Locate and identify every blood parasite.
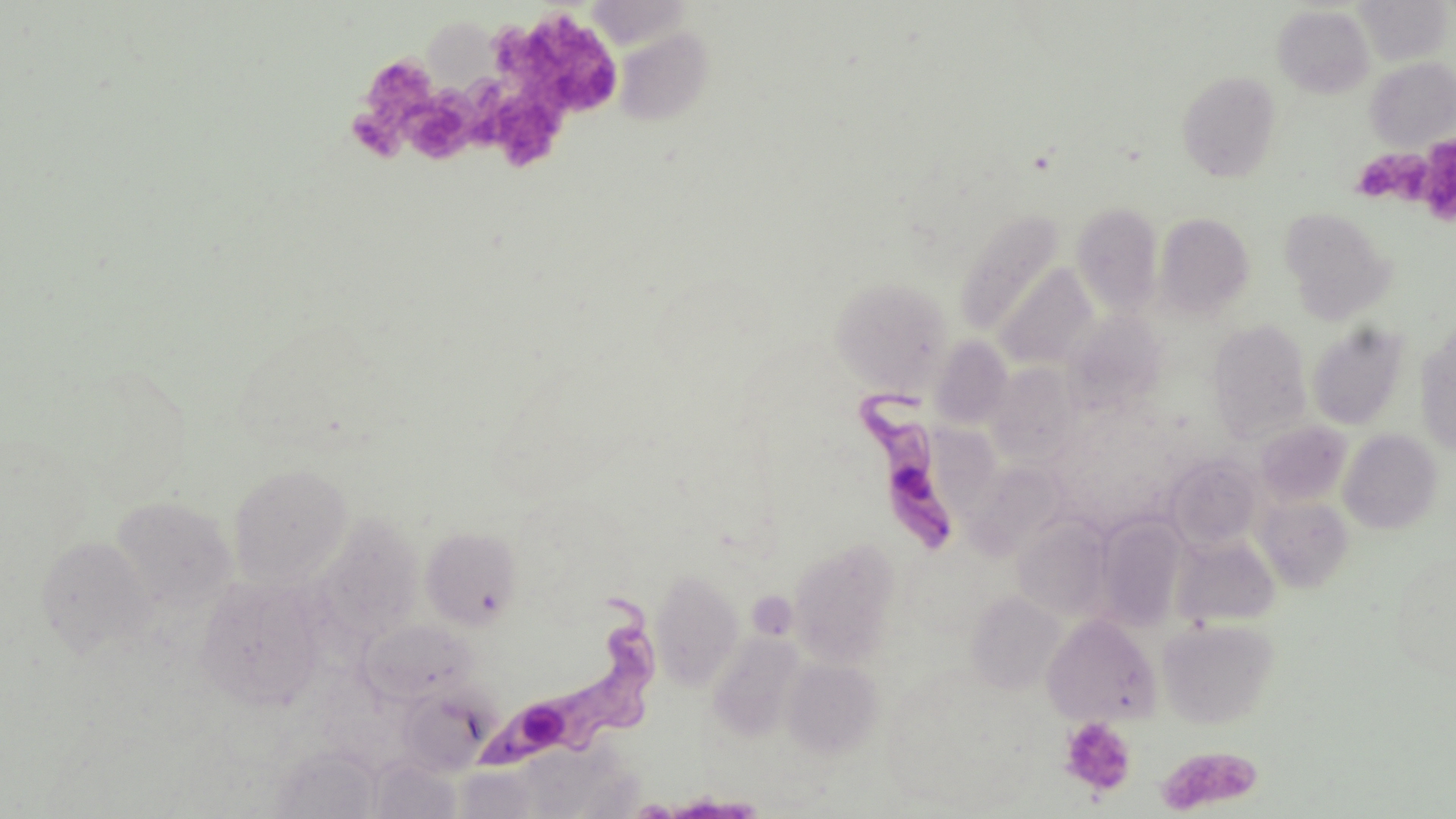

Approximate bounding boxes as (x1, y1, x2, y2) in pixels.
Trypanosoma brucei: (850, 385, 959, 558), (491, 595, 657, 769).
No Plasmodium falciparum, Plasmodium ovale, Plasmodium malariae, Plasmodium vivax, or Babesia divergens observed.

slide_level_diagnosis: Trypanosoma brucei
preparation: thin blood film
platelet_locations: 'approximate bounding boxes as (x1, y1, x2, y2) in pixels: (492, 9, 618, 116), (363, 55, 437, 117), (475, 85, 568, 171), (402, 94, 475, 164), (353, 108, 409, 164), (1417, 134, 1456, 223), (1353, 148, 1437, 208), (1059, 716, 1137, 797), (1157, 745, 1263, 815)'
uninfected_red_blood_cell_locations: 'approximate bounding boxes as (x1, y1, x2, y2) in pixels: (1356, 0, 1451, 65), (1273, 5, 1374, 97), (426, 13, 505, 94), (614, 27, 714, 126), (1366, 57, 1456, 150), (1177, 71, 1282, 181), (1071, 202, 1164, 315), (1279, 208, 1396, 323), (955, 209, 1065, 336), (1153, 212, 1255, 320), (995, 263, 1098, 370), (831, 276, 954, 392), (1064, 310, 1166, 415), (1207, 320, 1314, 442), (1306, 322, 1410, 430), (1415, 329, 1456, 456), (930, 336, 1013, 429), (986, 363, 1080, 464), (1255, 420, 1352, 507), (1338, 429, 1443, 534), (1164, 453, 1264, 552), (966, 462, 1067, 556), (227, 463, 353, 589), (110, 495, 237, 615), (1254, 495, 1354, 592), (1095, 514, 1190, 632), (1013, 515, 1115, 622), (421, 526, 523, 630), (36, 534, 157, 660), (1170, 534, 1280, 629), (787, 538, 903, 668), (1390, 550, 1455, 682), (650, 568, 744, 690), (194, 574, 326, 710), (746, 589, 797, 642), (966, 590, 1066, 695), (1041, 613, 1161, 725), (1157, 618, 1280, 729), (361, 619, 479, 705), (707, 631, 806, 742), (782, 658, 882, 758), (396, 684, 493, 775), (503, 739, 641, 818), (270, 743, 383, 819), (368, 756, 463, 818), (452, 765, 548, 819)'
image_size: 1456×819 pixels
modality: optical microscopy
field_of_view: single
magnification: 1000x
stain: May-Grünwald-Giemsa